State which parasite is depicted.
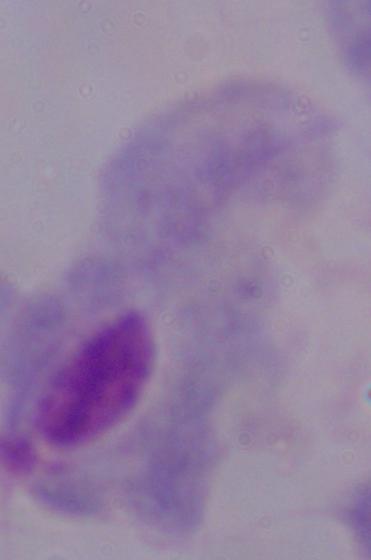

This is a trichomonad.

Captured at 1000x magnification. Micrograph.